Mark where platelets are.
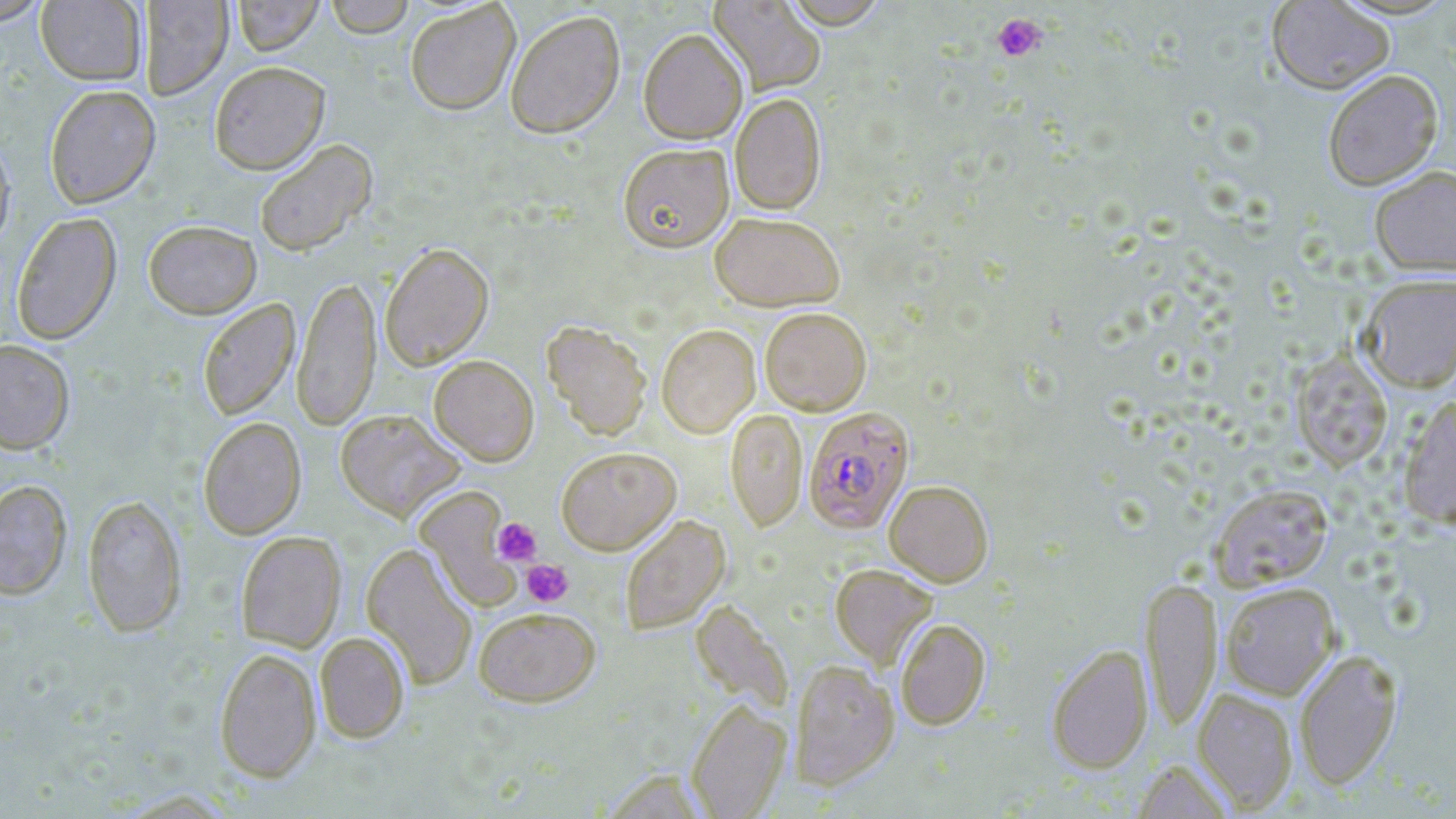

Approximate bounding boxes as (x1,y1)-(x2,y2) corner pairs in pixels.
Platelets: (992,13)-(1047,62), (492,518)-(542,566), (521,559)-(573,606).

{
  "slide_level_diagnosis": "Plasmodium falciparum",
  "field_of_view": "single",
  "uninfected_red_blood_cell_locations": "approximate bounding boxes as (x1,y1)-(x2,y2) corner pairs in pixels: (0,0)-(50,25), (232,0)-(324,55), (324,0)-(416,37), (708,0)-(826,96), (779,0)-(891,28), (1266,0)-(1395,95), (36,1)-(146,85), (140,1)-(233,99), (404,1)-(521,115), (505,9)-(625,138), (638,28)-(748,144), (209,61)-(330,174), (1322,69)-(1443,190), (44,85)-(160,208), (730,93)-(827,214), (0,133)-(16,253), (254,139)-(377,256), (618,142)-(734,252), (1369,166)-(1456,276), (709,211)-(846,311), (12,212)-(122,345), (143,219)-(261,318), (379,242)-(494,370), (292,272)-(381,432), (1358,274)-(1456,391), (197,298)-(300,421), (759,306)-(871,416), (541,320)-(652,439), (656,324)-(760,437), (0,340)-(75,453), (1290,349)-(1393,471), (428,354)-(539,465), (1398,394)-(1456,529), (725,408)-(807,531), (335,409)-(464,521), (198,417)-(306,539), (555,446)-(681,554), (0,479)-(72,600), (884,479)-(994,586), (1209,483)-(1334,591), (415,486)-(523,607), (82,494)-(187,637), (619,514)-(730,635), (237,531)-(346,651), (362,542)-(477,690), (830,563)-(938,669), (1141,576)-(1222,732), (1219,582)-(1340,700), (691,600)-(793,715), (473,606)-(600,706), (895,618)-(990,730), (315,631)-(410,743), (1046,644)-(1153,773), (215,647)-(321,783), (1294,649)-(1403,790), (789,659)-(899,789), (1192,687)-(1299,812), (686,698)-(791,818), (1132,759)-(1235,819)",
  "stain": "May-Grünwald-Giemsa",
  "magnification": "1000x",
  "preparation": "thin blood smear",
  "modality": "optical microscopy",
  "image_size": "1456×819 pixels",
  "plasmodium_falciparum_infected_red_blood_cell_locations": "approximate bounding boxes as (x1,y1)-(x2,y2) corner pairs in pixels: (802,406)-(914,534)"
}